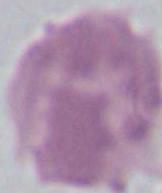 Micrograph. An erythrocyte is seen. 1000x magnification.